Name the parasite shown.
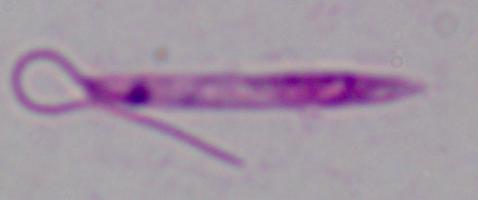
This is Leishmania.

magnification = 1000x
modality = photomicrograph